Describe the morphology of the red blood cells.
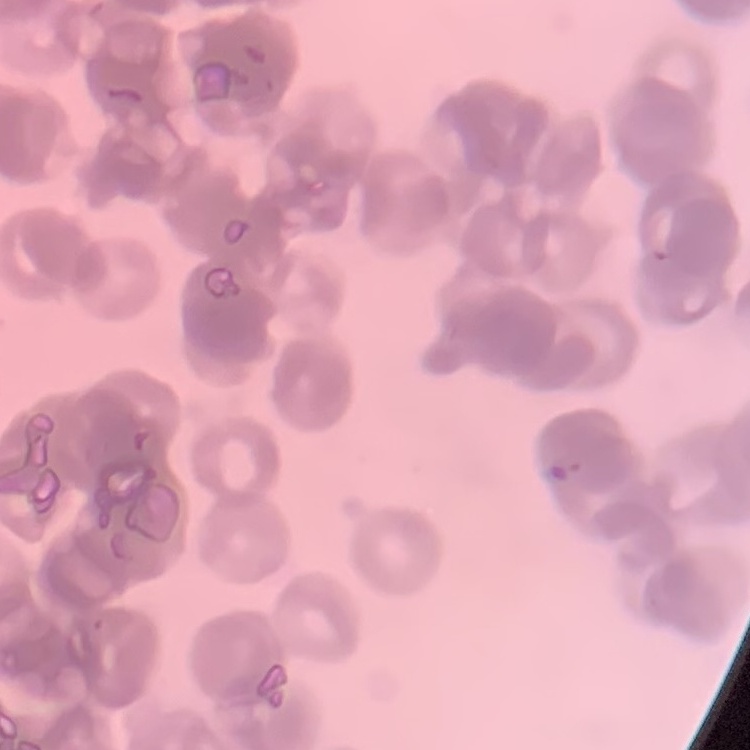
They show rouleaux formation.

Summary:
  - Preparation: thin blood film
  - Image type: one tile cut from a larger photomicrograph
  - Stain: Field's or Giemsa